Locate every Plasmodium falciparum-infected red blood cell.
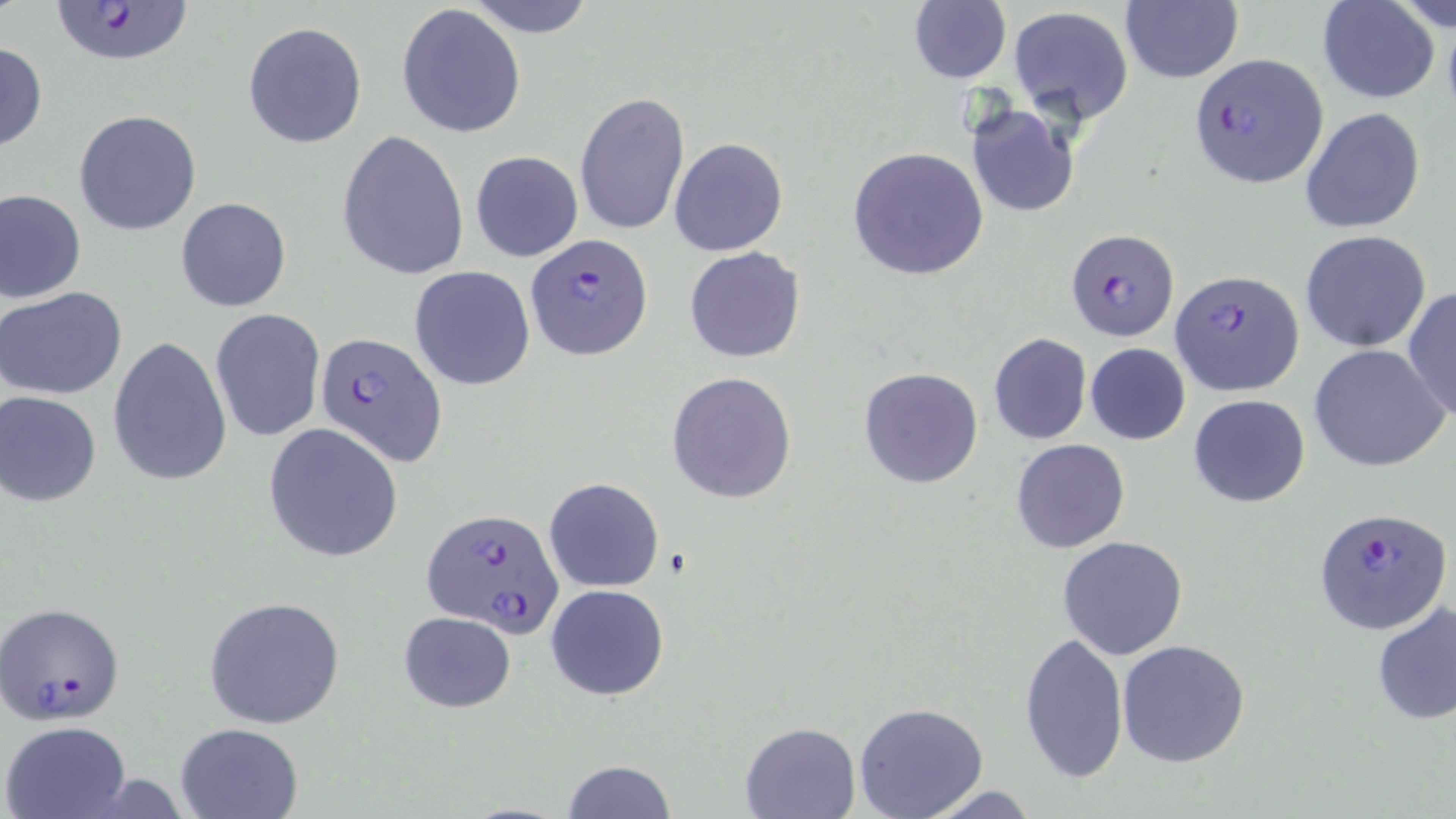

Approximate bounding boxes as [x1, y1, x2, y2] in pixels.
Plasmodium falciparum-infected red blood cells: [45, 1, 198, 68], [1189, 54, 1328, 186], [1065, 228, 1180, 341], [526, 233, 653, 358], [1171, 267, 1304, 396], [314, 332, 447, 465], [1313, 504, 1453, 635], [422, 506, 561, 635], [0, 602, 126, 723].

{
  "slide_level_diagnosis": "Plasmodium falciparum",
  "preparation": "thin blood smear",
  "magnification": "1000x",
  "image_size": "1456×819 pixels",
  "uninfected_red_blood_cell_locations": "approximate bounding boxes as [x1, y1, x2, y2] in pixels: [462, 0, 599, 37], [1317, 0, 1441, 103], [1388, 1, 1455, 34], [907, 2, 1011, 84], [1119, 2, 1243, 85], [397, 3, 526, 138], [1009, 6, 1131, 120], [243, 21, 367, 148], [0, 41, 46, 153], [574, 91, 690, 235], [964, 102, 1079, 218], [1301, 106, 1427, 235], [75, 110, 202, 234], [338, 129, 470, 280], [669, 137, 787, 256], [847, 148, 989, 280], [470, 150, 583, 262], [0, 189, 86, 304], [176, 198, 290, 312], [1300, 230, 1433, 353], [684, 246, 805, 362], [409, 266, 536, 391], [1, 286, 129, 400], [1403, 286, 1456, 421], [210, 308, 325, 441], [987, 332, 1091, 445], [108, 335, 232, 487], [1084, 343, 1191, 444], [1308, 344, 1450, 471], [858, 367, 984, 488], [667, 371, 797, 504], [0, 391, 102, 506], [1188, 393, 1310, 508], [263, 422, 404, 563], [1010, 439, 1130, 554], [543, 477, 665, 593], [1057, 535, 1189, 661], [545, 585, 670, 700], [203, 596, 345, 729], [1372, 600, 1455, 726], [397, 612, 515, 712], [1018, 631, 1128, 782], [1116, 638, 1250, 767], [852, 701, 989, 819], [1, 720, 131, 819], [174, 721, 303, 819], [739, 721, 861, 818], [559, 760, 677, 818], [914, 783, 1044, 818]",
  "field_of_view": "single",
  "stain": "May-Grünwald-Giemsa",
  "modality": "light microscopy"
}